Report the malaria status of this cell.
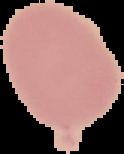
Uninfected.

Summary:
  - Preparation: thin blood smear
  - Image type: cell region segmented out of the field of view; surrounding area masked to black
  - Image size: 124×154 pixels